Assess this cell for malaria.
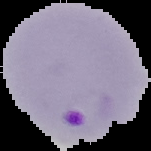

Parasitized.

Image is 151×151 pixels. From a thin blood smear. Segmented cell region on a black background.